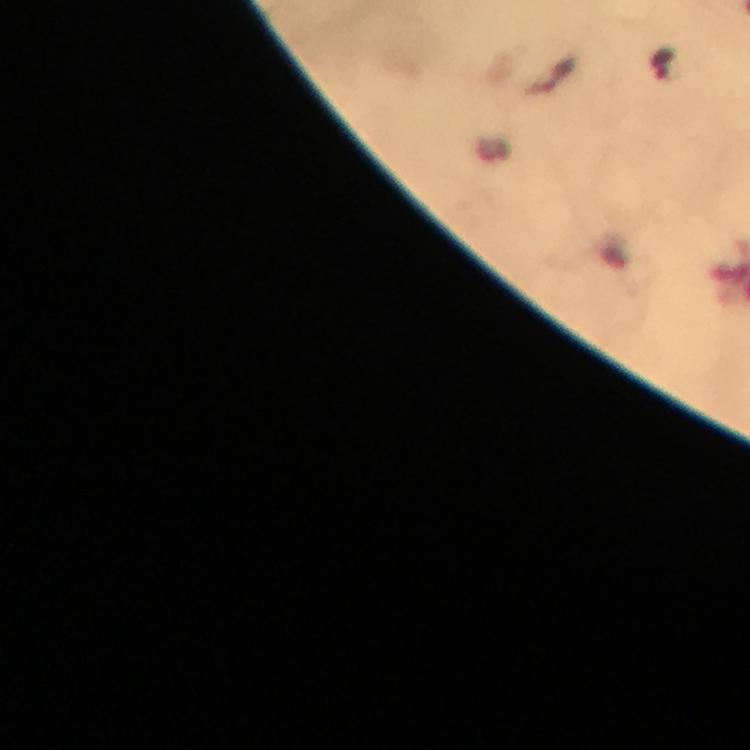
stain: Giemsa
image_size: 750×750 pixels
plasmodium_parasite_locations: 'approximate centers as [x, y] in pixels: [663, 68]'
cropped_from: one field of view
preparation: thick blood smear
capture: smartphone mounted on the microscope
immersion_oil: applied
context: from a malaria diagnostic workup
magnification: 100x